Classify this cell by malaria status.
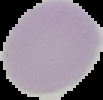
It is uninfected.

Summary:
  - Image size: 103×100 pixels
  - Preparation: thin blood smear
  - Image type: segmented cell region on a black background